Give the location of every parasitized red blood cell.
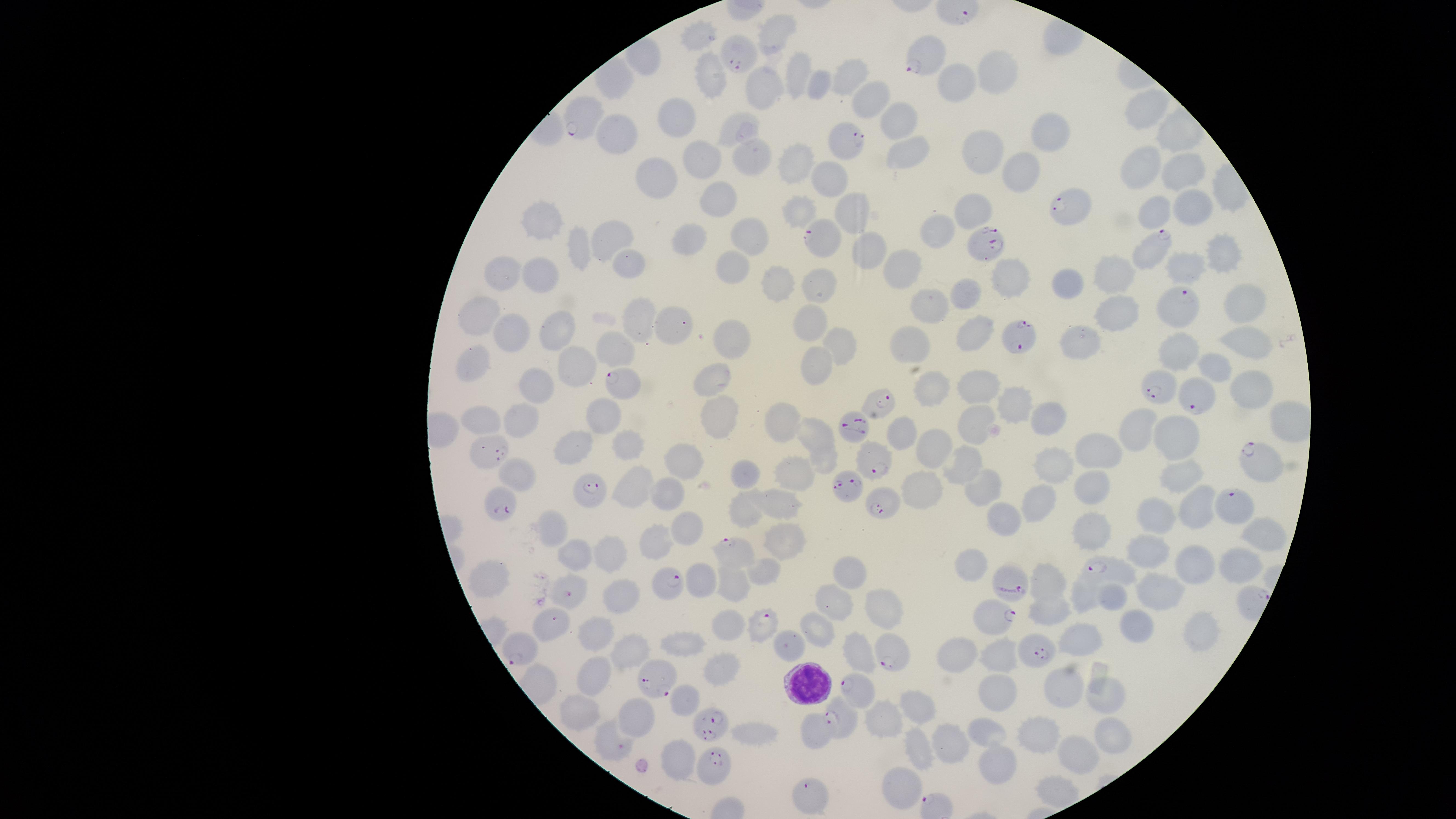

Approximate marker points as {x, y} in pixels.
Parasitized red blood cells: {738, 54}, {923, 60}, {583, 115}, {848, 145}, {1074, 208}, {820, 237}, {983, 241}, {1151, 248}, {1176, 301}, {1019, 338}, {627, 385}, {1159, 387}, {1198, 395}, {882, 403}, {854, 424}, {494, 450}, {874, 462}, {1259, 463}, {843, 484}, {593, 489}, {500, 500}, {886, 505}, {1236, 505}, {733, 552}, {1100, 566}, {673, 584}, {1013, 584}, {995, 617}, {554, 619}, {763, 625}, {525, 646}, {1034, 650}, {895, 659}, {661, 679}, {856, 688}, {841, 715}, {710, 720}, {609, 745}, {715, 769}, {813, 797}.

Approximate marker points as {x, y} in pixels. Uninfected red blood cells: {776, 35}, {691, 36}, {850, 73}, {998, 73}, {801, 74}, {709, 77}, {961, 82}, {770, 85}, {824, 86}, {870, 96}, {1148, 104}, {676, 116}, {898, 121}, {738, 128}, {1053, 130}, {619, 131}, {907, 148}, {980, 150}, {689, 156}, {749, 158}, {797, 160}, {1023, 169}, {1139, 169}, {1179, 174}, {652, 177}, {832, 183}, {721, 194}, {1194, 201}, {973, 207}, {803, 211}, {1154, 212}, {552, 217}, {844, 217}, {946, 226}, {746, 237}, {622, 238}, {697, 241}, {581, 248}, {865, 249}, {1220, 257}, {633, 261}, {546, 265}, {735, 266}, {1182, 267}, {506, 272}, {902, 274}, {1002, 275}, {1115, 276}, {780, 277}, {822, 281}, {1068, 286}, {970, 296}, {1241, 299}, {936, 305}, {1112, 308}, {485, 311}, {642, 318}, {814, 319}, {676, 325}, {558, 329}, {511, 330}, {735, 337}, {968, 337}, {1080, 340}, {840, 341}, {1248, 342}, {914, 344}, {1177, 348}, {617, 350}, {475, 361}, {812, 361}, {1215, 362}, {577, 364}, {971, 381}, {538, 386}, {715, 388}, {936, 388}, {1250, 390}, {1015, 403}, {602, 414}, {485, 415}, {791, 415}, {520, 418}, {974, 419}, {1051, 420}, {721, 422}, {1144, 424}, {819, 430}, {909, 431}, {1179, 436}, {576, 440}, {939, 441}, {631, 443}, {1098, 447}, {685, 458}, {1053, 459}, {825, 461}, {960, 463}, {516, 473}, {793, 473}, {1184, 474}, {748, 477}, {636, 483}, {979, 485}, {670, 488}, {1098, 488}, {927, 492}, {1042, 502}, {774, 504}, {1198, 506}, {744, 508}, {1006, 513}, {1153, 515}, {687, 525}, {1092, 531}, {554, 532}, {1260, 533}, {788, 536}, {654, 541}, {1146, 551}, {575, 552}, {611, 555}, {1197, 558}, {1242, 559}, {977, 569}, {769, 571}, {848, 575}, {1048, 579}, {490, 584}, {731, 584}, {1162, 585}, {615, 593}, {1086, 594}, {1114, 595}, {837, 601}, {881, 604}, {1045, 609}, {1200, 624}, {821, 626}, {724, 627}, {1132, 627}, {592, 630}, {1083, 637}, {685, 643}, {857, 649}, {956, 652}, {630, 654}, {995, 656}, {719, 667}, {592, 668}, {1062, 684}, {996, 690}, {1103, 691}, {689, 699}, {923, 705}, {582, 706}, {637, 715}, {881, 723}, {816, 728}, {991, 728}, {1043, 729}, {756, 732}, {1109, 733}, {952, 740}, {923, 753}, {1075, 755}, {675, 762}, {1000, 769}, {900, 787}, {1057, 787}. White blood cells: {807, 682}. Circular visible region. Photographed with a smartphone camera through the microscope eyepiece. Thin smear of blood. One field of view of the specimen. Species: Plasmodium falciparum. Giemsa-stained preparation. Image is 1456×819 pixels.